Comment on the morphology of the red blood cells.
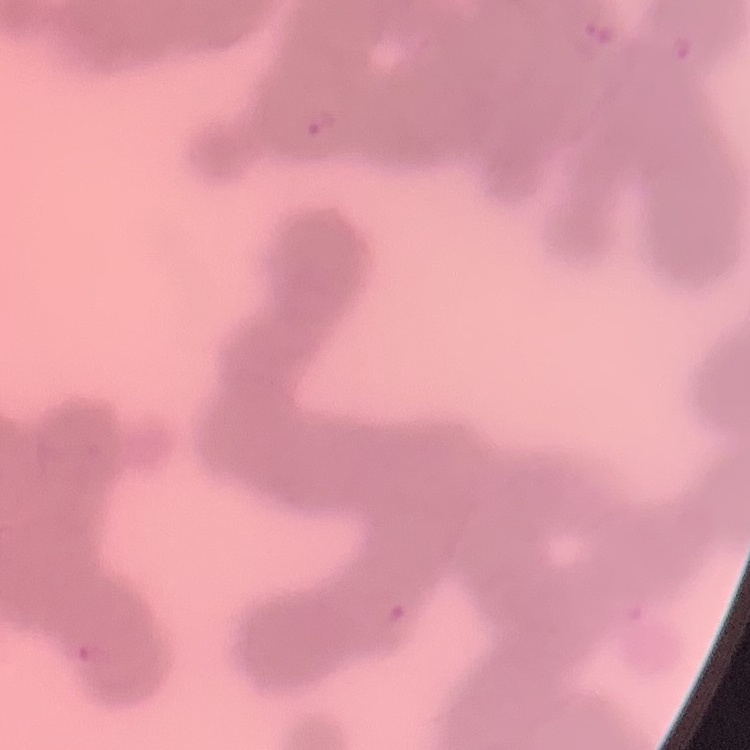
Rouleaux formation.

Stained with either Field's or Giemsa. Square crop of a larger photomicrograph. Thin blood smear.